Report the malaria status of this cell.
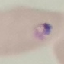

It is parasitized.

{
  "stain": "Giemsa",
  "image_type": "automatically extracted cell patch, resized to 64 × 64 pixels",
  "preparation": "thin blood smear",
  "capture": "smartphone camera at the microscope eyepiece"
}